Name the parasite shown.
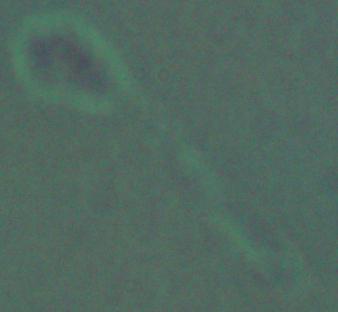
This is Leishmania.

1000x magnification. Micrograph.